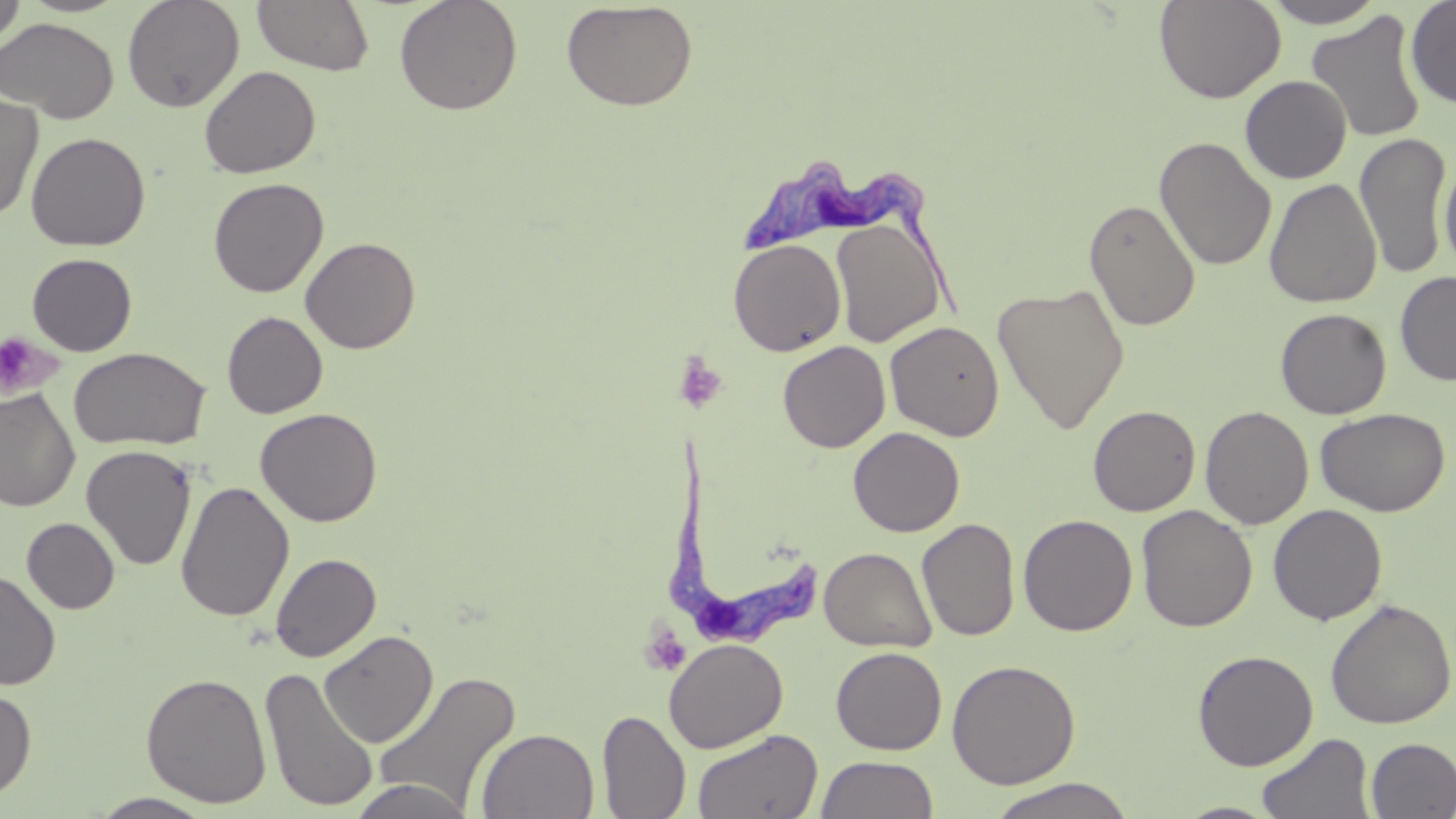

Summary:
  - Coordinate format: approximate bounding boxes as [x1, y1, x2, y2] in pixels
  - Uninfected red blood cell locations: [0, 0, 26, 49], [122, 0, 245, 113], [394, 0, 523, 116], [1154, 0, 1286, 104], [1261, 0, 1389, 28], [1405, 0, 1456, 108], [251, 1, 375, 76], [561, 2, 699, 111], [1306, 11, 1428, 144], [0, 18, 118, 123], [199, 65, 321, 178], [1240, 75, 1352, 184], [0, 93, 43, 223], [26, 132, 150, 251], [1354, 133, 1451, 279], [1154, 137, 1277, 271], [1439, 154, 1455, 274], [208, 177, 328, 298], [1264, 178, 1382, 308], [1084, 198, 1201, 331], [830, 216, 946, 347], [300, 236, 421, 354], [727, 238, 847, 357], [26, 253, 137, 357], [1395, 270, 1456, 387], [992, 282, 1130, 434], [1275, 308, 1391, 419], [222, 311, 328, 419], [885, 321, 1004, 441], [778, 341, 891, 453], [68, 347, 210, 450], [0, 388, 80, 512], [1088, 404, 1201, 516], [1200, 406, 1314, 529], [1315, 407, 1450, 517], [255, 408, 383, 527], [848, 426, 965, 537], [81, 444, 197, 571], [176, 480, 294, 622], [1268, 504, 1387, 625], [1136, 505, 1257, 633], [1017, 513, 1138, 636], [21, 517, 119, 614], [917, 517, 1020, 642], [819, 547, 936, 653], [270, 552, 381, 662], [0, 570, 60, 690], [1325, 597, 1456, 730], [318, 629, 438, 747], [664, 638, 788, 753], [831, 646, 947, 755], [1193, 649, 1318, 771], [946, 659, 1082, 789], [259, 666, 379, 812], [373, 669, 522, 813], [140, 672, 272, 808], [0, 686, 36, 800], [597, 708, 691, 819], [476, 728, 599, 818], [692, 728, 823, 819], [1255, 733, 1375, 819], [1366, 738, 1456, 818], [815, 754, 940, 818], [348, 778, 476, 819], [983, 778, 1141, 819], [89, 792, 217, 818], [1172, 801, 1284, 818]
  - Platelet locations: [0, 331, 58, 398], [672, 352, 727, 413], [640, 625, 692, 677]
  - Trypanosoma brucei locations: [742, 154, 966, 317], [658, 434, 818, 648]
  - Slide-level diagnosis: Trypanosoma brucei
  - Preparation: thin blood film
  - Magnification: 1000x
  - Stain: May-Grünwald-Giemsa
  - Image size: 1456×819 pixels
  - Field of view: one of a larger specimen
  - Modality: light microscopy